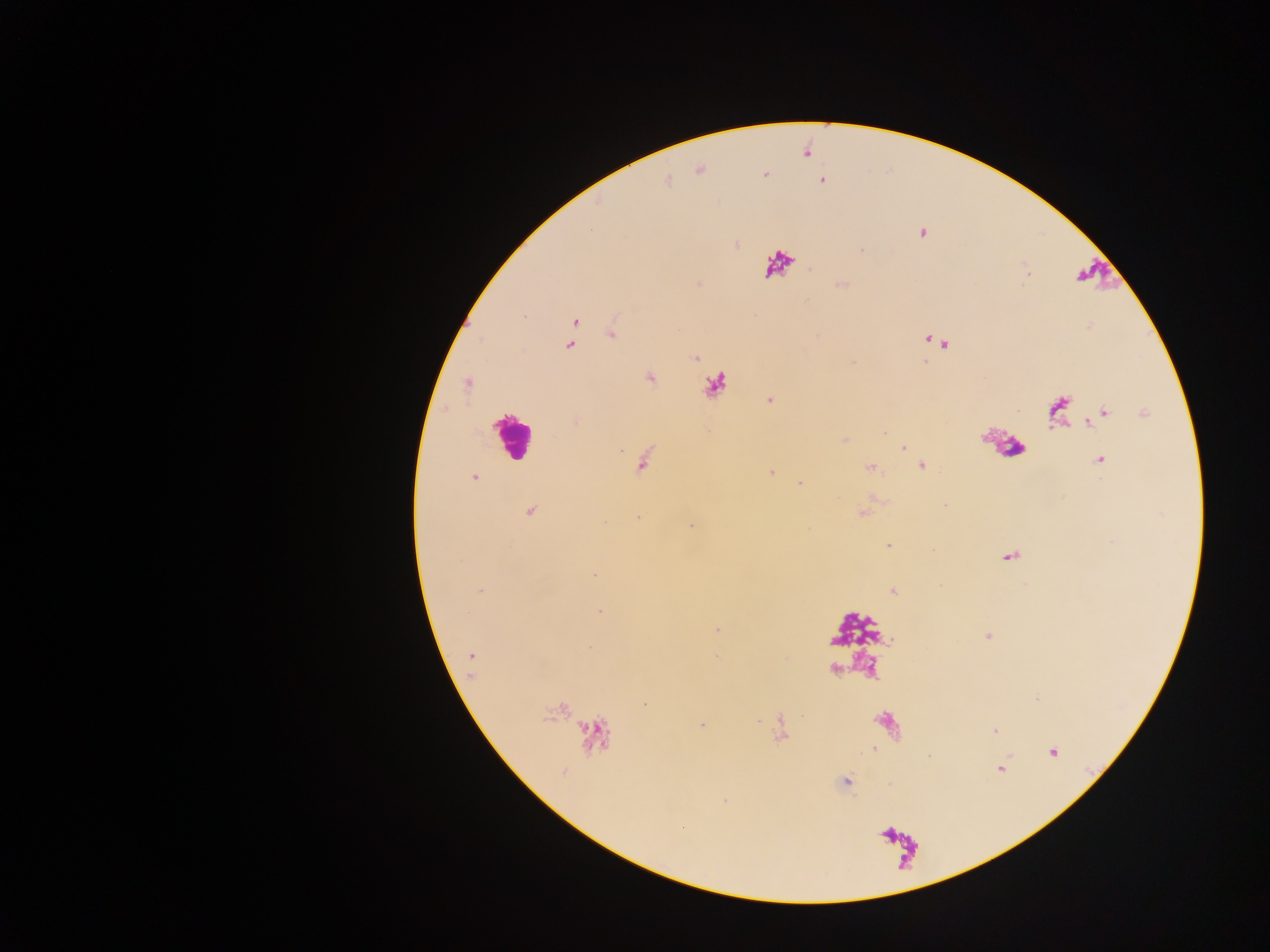
Approximate centers as x y in pixels.
Summary:
  - Leukocyte locations: 779 264; 509 436
  - Malaria parasite locations: 821 181; 922 233; 574 322; 611 333; 937 341; 570 345; 695 359; 649 377; 468 383; 770 401; 1100 416; 904 448; 1101 460; 921 466; 870 468; 772 473; 474 477; 800 483; 530 512; 638 517; 691 525; 888 545; 595 574; 480 590; 892 590; 600 612; 717 629; 987 636; 589 649; 472 656; 645 704; 701 724; 995 730; 1052 752; 929 755; 1000 769; 845 782; 726 800; 682 827
  - Preparation: thick blood smear
  - Country: Ghana
  - Image size: 1270×952 pixels
  - Capture: mobile-phone photograph through a microscope
  - Field of view: single